Assess this cell for malaria.
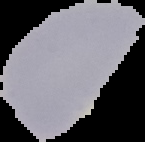
It is uninfected.

Summary:
  - Preparation: thin blood smear
  - Image type: cell region segmented out of the field of view; surrounding area masked to black
  - Image size: 145×142 pixels